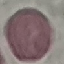

Summary:
  - Result: no malaria parasites detected
  - Stain: Giemsa
  - Preparation: thin blood smear
  - Capture: smartphone camera at the microscope eyepiece
  - Image type: automatically extracted cell patch, resized to 64 × 64 pixels